Assess this cell for malaria.
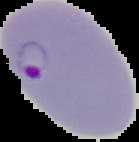

It is parasitized.

Summary:
  - Image size: 139×142 pixels
  - Image type: segmented cell region with the area outside set to black
  - Preparation: thin blood smear